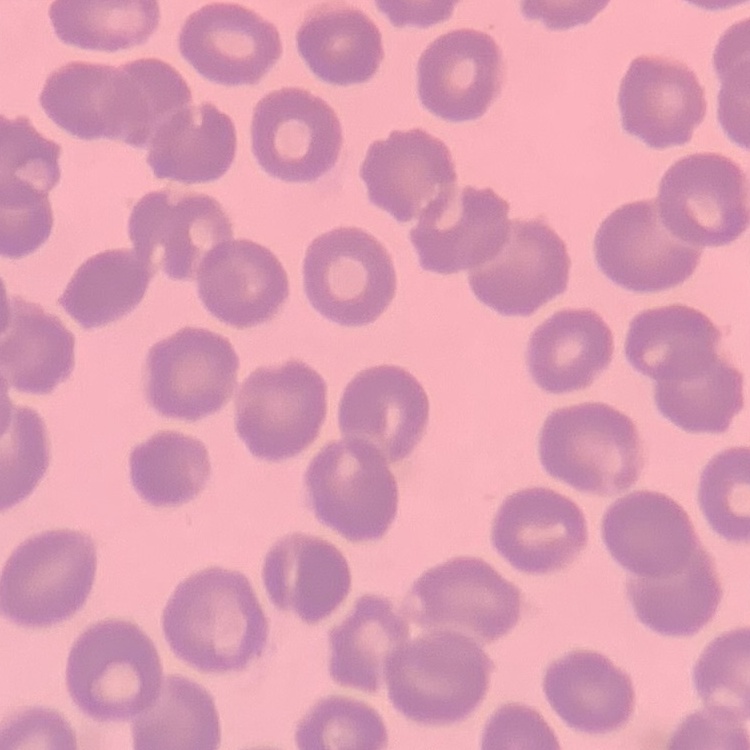

The erythrocytes exhibit no rouleaux formation. Field's or Giemsa stain. One tile cut from a larger photomicrograph. Thin blood smear.